Report the malaria status of this cell.
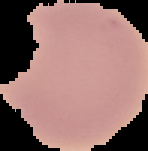

Uninfected.

Image is 148×151 pixels. From a thin blood film. Cell region segmented out of the field of view; the surrounding area is masked to black.